Comment on the morphology of the erythrocytes.
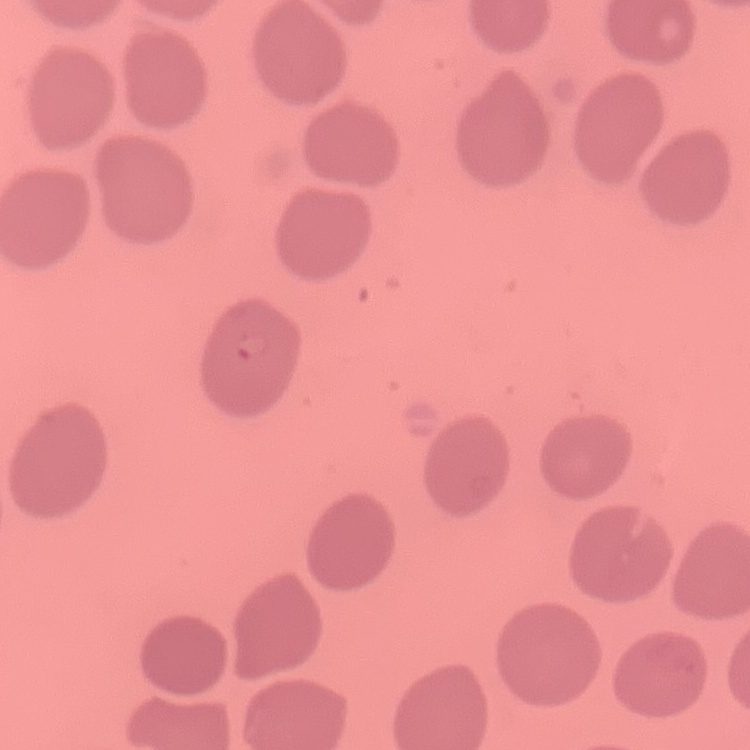

They show no rouleaux formation.

Stained with either Field's or Giemsa. One tile cut from a larger photomicrograph. Thin peripheral smear.